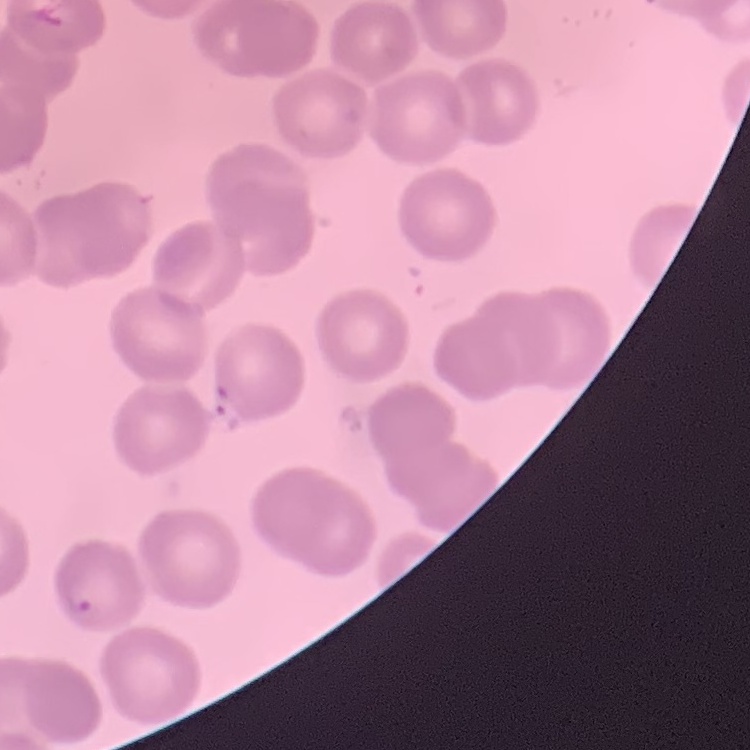
Summary:
  - Red blood cell morphology: no rouleaux formation
  - Preparation: thin blood smear
  - Image type: square crop of a larger photomicrograph
  - Stain: Field's or Giemsa